Classify this cell by malaria status.
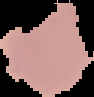

It is uninfected.

image size = 94×97 pixels
image type = cell region segmented out of the field of view; surrounding area masked to black
preparation = thin blood smear